Give the position of every malaria parasite.
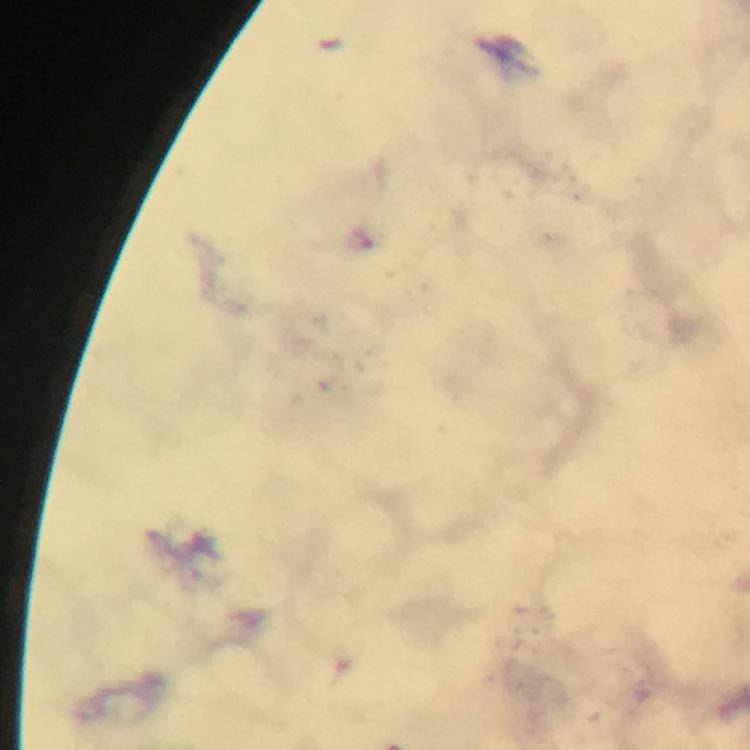

Approximate centers as {x, y} in pixels.
Malaria parasites: {361, 240}.

Summary:
  - Immersion oil: applied
  - Preparation: thick blood film
  - Capture: smartphone photograph through a microscope
  - Cropped from: a single field of view
  - Magnification: 100x
  - Context: from a diagnostic examination for malaria
  - Image size: 750×750 pixels
  - Stain: Giemsa